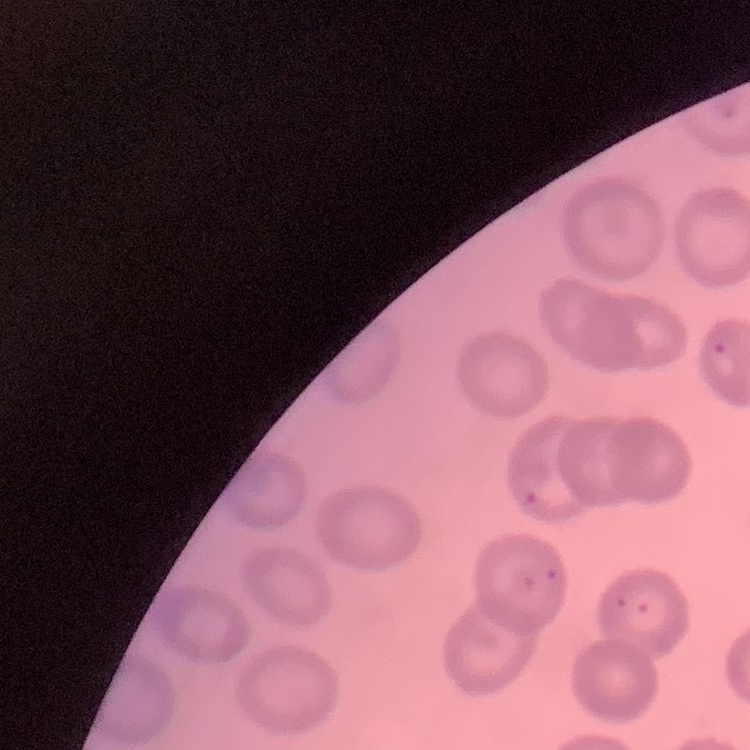
The red blood cells exhibit no rouleaux formation. Thin peripheral smear. Field's or Giemsa stain. One tile cut from a larger photomicrograph.